State which cell type is depicted.
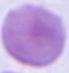
An erythrocyte.

magnification: 1000x
modality: photomicrograph